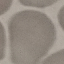 Result: negative for malaria parasites. Acquired by smartphone through the microscope eyepiece. Giemsa-stained preparation. Thin blood film. Automatically extracted cell patch, resized to 64 × 64 pixels.